Identify the blood parasite species.
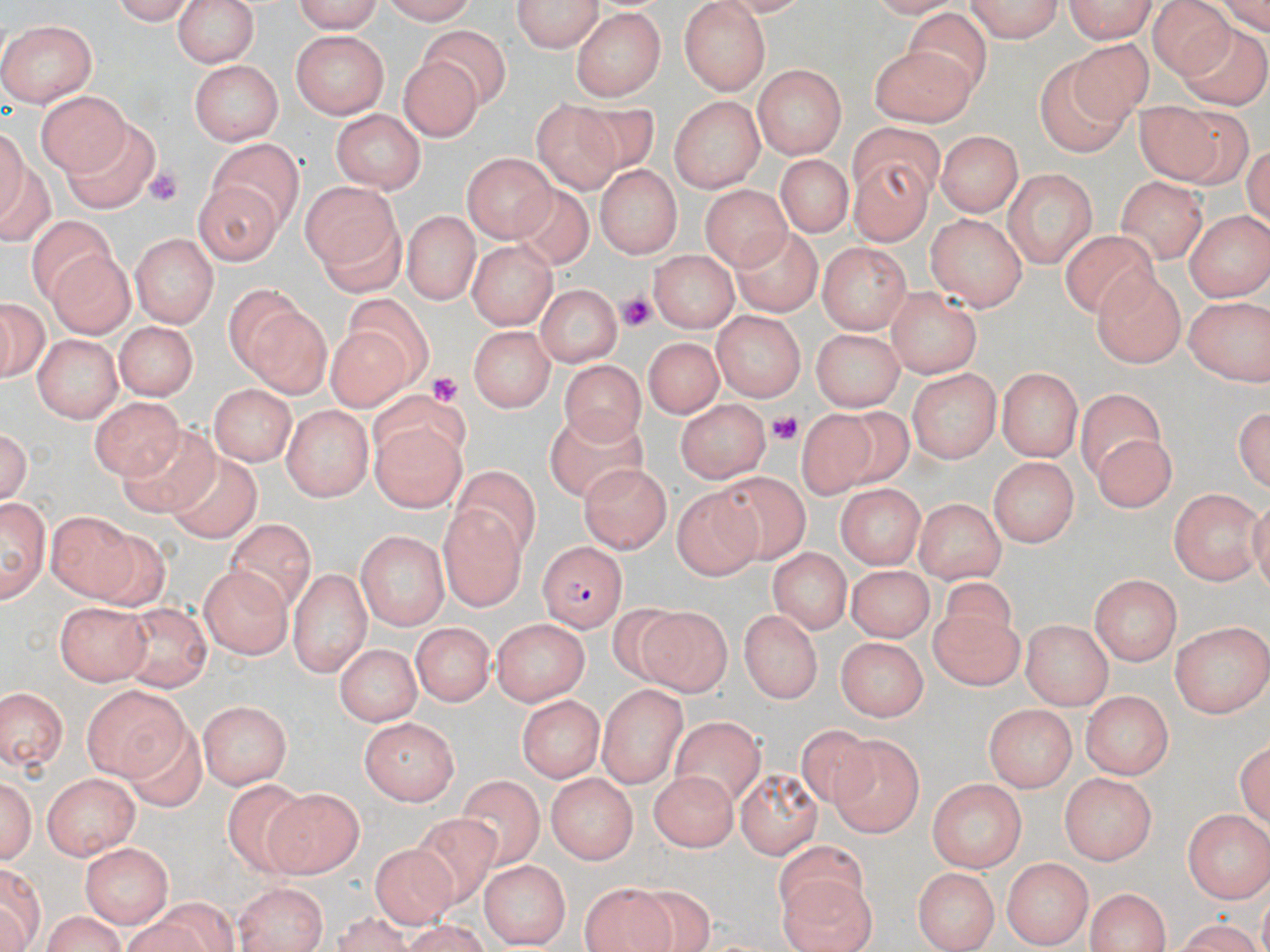

Plasmodium falciparum.

Summary:
  - Coordinate format: approximate bounding boxes as (x1, y1, x2, y2) in pixels
  - Platelet locations: (141, 167, 184, 206), (614, 285, 657, 334), (427, 372, 461, 408), (769, 411, 805, 445)
  - Uninfected red blood cell locations: (171, 0, 263, 66), (289, 0, 383, 31), (381, 0, 484, 23), (510, 0, 604, 53), (964, 0, 1069, 42), (1065, 0, 1160, 45), (102, 1, 195, 23), (676, 1, 769, 93), (1148, 2, 1235, 76), (903, 4, 993, 100), (571, 11, 664, 100), (4, 17, 99, 105), (1174, 20, 1270, 112), (418, 28, 511, 111), (292, 30, 388, 119), (1068, 37, 1150, 126), (189, 47, 362, 136), (869, 47, 981, 127), (401, 57, 485, 139), (1034, 58, 1131, 157), (191, 61, 281, 143), (750, 65, 848, 156), (38, 88, 129, 176), (668, 95, 766, 189), (529, 97, 622, 201), (1128, 98, 1225, 186), (568, 101, 662, 171), (331, 110, 425, 194), (1171, 110, 1256, 191), (64, 119, 155, 216), (844, 120, 949, 198), (1, 128, 47, 245), (933, 132, 1021, 217), (208, 137, 304, 227), (462, 152, 556, 241), (846, 155, 934, 251), (772, 158, 851, 240), (593, 164, 680, 259), (1003, 169, 1098, 268), (196, 173, 291, 265), (1118, 175, 1209, 257), (296, 179, 405, 291), (508, 185, 595, 270), (703, 185, 789, 271), (399, 206, 485, 308), (1185, 206, 1270, 298), (31, 213, 118, 310), (924, 213, 1026, 310), (731, 226, 822, 317), (1060, 230, 1159, 323), (131, 235, 215, 326), (465, 239, 559, 335), (817, 241, 912, 332), (651, 246, 736, 331), (46, 247, 135, 337), (1093, 271, 1187, 367), (227, 284, 335, 396), (534, 284, 621, 366), (886, 289, 986, 375), (1184, 292, 1270, 384), (343, 294, 432, 389), (0, 296, 48, 386), (710, 309, 804, 400), (113, 320, 196, 402), (467, 324, 555, 412), (813, 325, 907, 410), (319, 326, 415, 418), (34, 335, 120, 421), (643, 336, 723, 419), (563, 359, 645, 453), (908, 366, 1000, 463), (995, 367, 1085, 458), (208, 383, 294, 466), (1077, 387, 1161, 483), (367, 391, 473, 477), (91, 396, 180, 479), (1234, 397, 1269, 497), (676, 399, 770, 482), (282, 402, 370, 501), (550, 405, 650, 504), (828, 408, 919, 483), (796, 409, 876, 503), (1, 423, 36, 508), (117, 425, 225, 518), (371, 428, 460, 514), (1087, 435, 1177, 505), (170, 454, 257, 546), (989, 456, 1082, 549), (581, 461, 675, 549), (449, 462, 541, 558), (709, 472, 821, 568), (833, 483, 927, 567), (670, 486, 764, 585), (1170, 486, 1264, 587), (0, 494, 49, 600), (911, 498, 1008, 579), (439, 505, 525, 610), (48, 508, 146, 604), (224, 521, 318, 621), (356, 529, 448, 632), (87, 530, 182, 612), (771, 544, 853, 636), (197, 564, 292, 659), (846, 564, 933, 639), (287, 565, 372, 673), (1088, 572, 1183, 664), (941, 575, 1019, 644), (56, 600, 149, 683), (127, 603, 209, 691), (638, 605, 735, 701), (739, 609, 824, 702), (926, 610, 1024, 692), (493, 617, 591, 707), (1021, 620, 1114, 708), (1172, 620, 1270, 716), (409, 624, 490, 710), (837, 635, 928, 723), (332, 642, 419, 726), (81, 681, 189, 777), (596, 683, 685, 786), (0, 689, 69, 774), (1085, 692, 1172, 780), (519, 693, 602, 784), (196, 700, 294, 786), (984, 705, 1078, 793), (361, 716, 458, 807), (116, 717, 208, 819), (665, 719, 766, 815), (796, 721, 885, 808), (826, 733, 923, 836), (1233, 736, 1270, 836), (735, 767, 822, 856), (0, 769, 39, 869), (40, 769, 140, 859), (547, 771, 639, 863), (647, 771, 740, 848), (1059, 772, 1158, 866), (927, 777, 1029, 868), (455, 778, 550, 871), (220, 780, 319, 880), (267, 788, 362, 878), (1184, 808, 1270, 900), (405, 812, 502, 911), (775, 836, 875, 928), (80, 841, 176, 927), (368, 845, 457, 932), (1003, 858, 1093, 946), (481, 859, 572, 948), (913, 866, 997, 950), (0, 867, 48, 936), (776, 875, 880, 952), (624, 881, 723, 950), (232, 882, 329, 952), (579, 882, 671, 952), (1086, 889, 1174, 951), (149, 897, 241, 952), (333, 903, 414, 952), (38, 912, 130, 952), (1165, 917, 1265, 951)
  - Plasmodium falciparum-infected red blood cell locations: (537, 542, 626, 632)
  - Modality: light microscopy
  - Magnification: 1000x
  - Stain: May-Grünwald-Giemsa
  - Preparation: thin blood smear
  - Image size: 1270×952 pixels
  - Field of view: one of a larger specimen